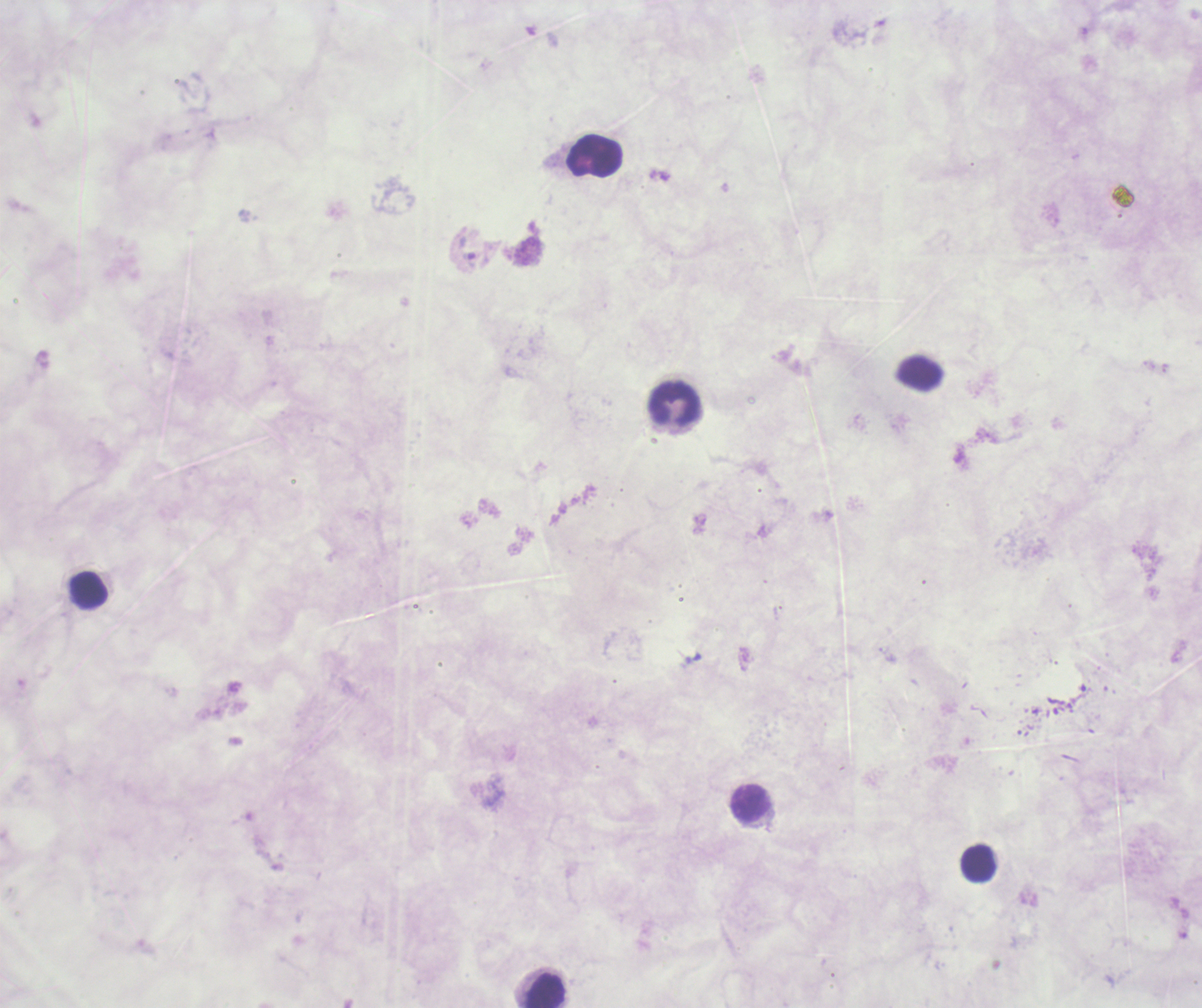

Approximate centers as [x, y] in pixels. Trophozoite locations: [467, 248]. Leukocyte locations: [596, 156], [919, 371], [675, 403], [88, 590], [750, 804], [978, 863], [545, 991]. Image is 1202×1008 pixels. Romanowsky-stained preparation. Previously used in an actual diagnosis. Captured at 100x magnification. Thick blood smear. Coloration quality: bad. Result: Plasmodium parasites identified. One field from this slide. Background quality: poor.